Name the parasite shown.
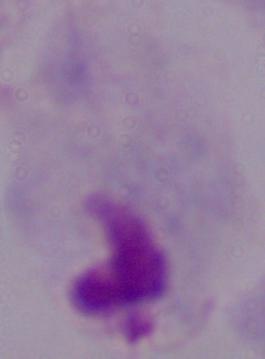

A trichomonad.

Summary:
  - Magnification: 1000x
  - Modality: micrograph